Locate every Plasmodium parasite.
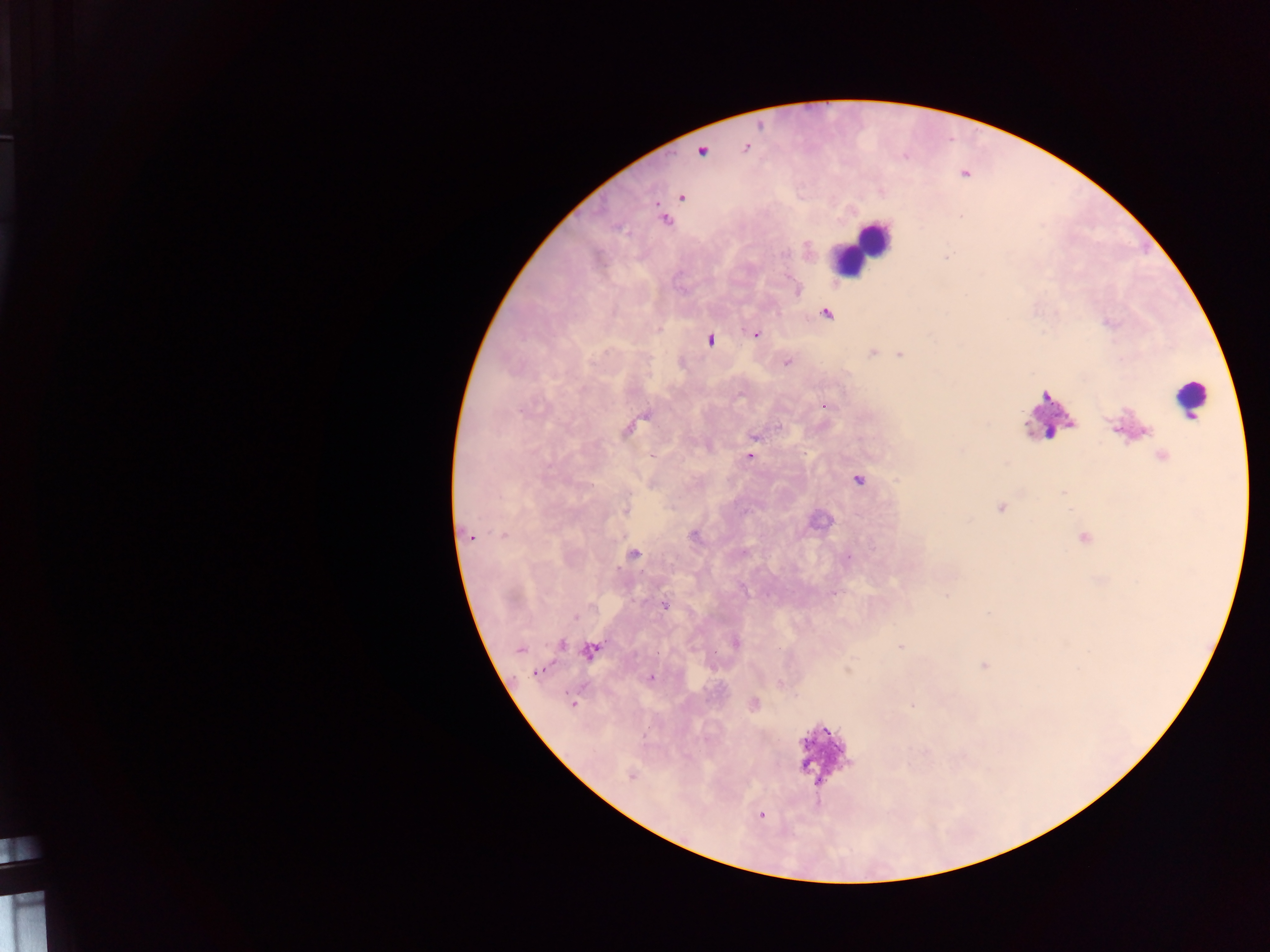
Approximate centers as [x, y] in pixels.
Plasmodium parasites: [745, 147], [702, 151], [681, 198], [664, 220], [826, 314], [756, 334], [709, 340], [872, 353], [900, 355], [787, 363], [825, 405], [647, 416], [779, 426], [627, 429], [754, 436], [749, 456], [1163, 456], [858, 479], [1001, 508], [625, 510], [504, 535], [694, 536], [471, 537], [633, 553], [848, 557], [947, 595], [592, 606], [666, 606], [575, 616], [735, 643], [562, 644], [901, 647], [519, 649], [590, 651], [538, 673], [651, 677], [573, 704], [754, 704], [631, 776], [760, 815].

Summary:
  - Leukocyte locations: [860, 247], [1189, 398], [1051, 414], [822, 760]
  - Country: Ghana
  - Field of view: single
  - Image size: 1270×952 pixels
  - Preparation: thick blood smear
  - Capture: mobile-phone photograph through a microscope